Outline each blood parasite and name the species.
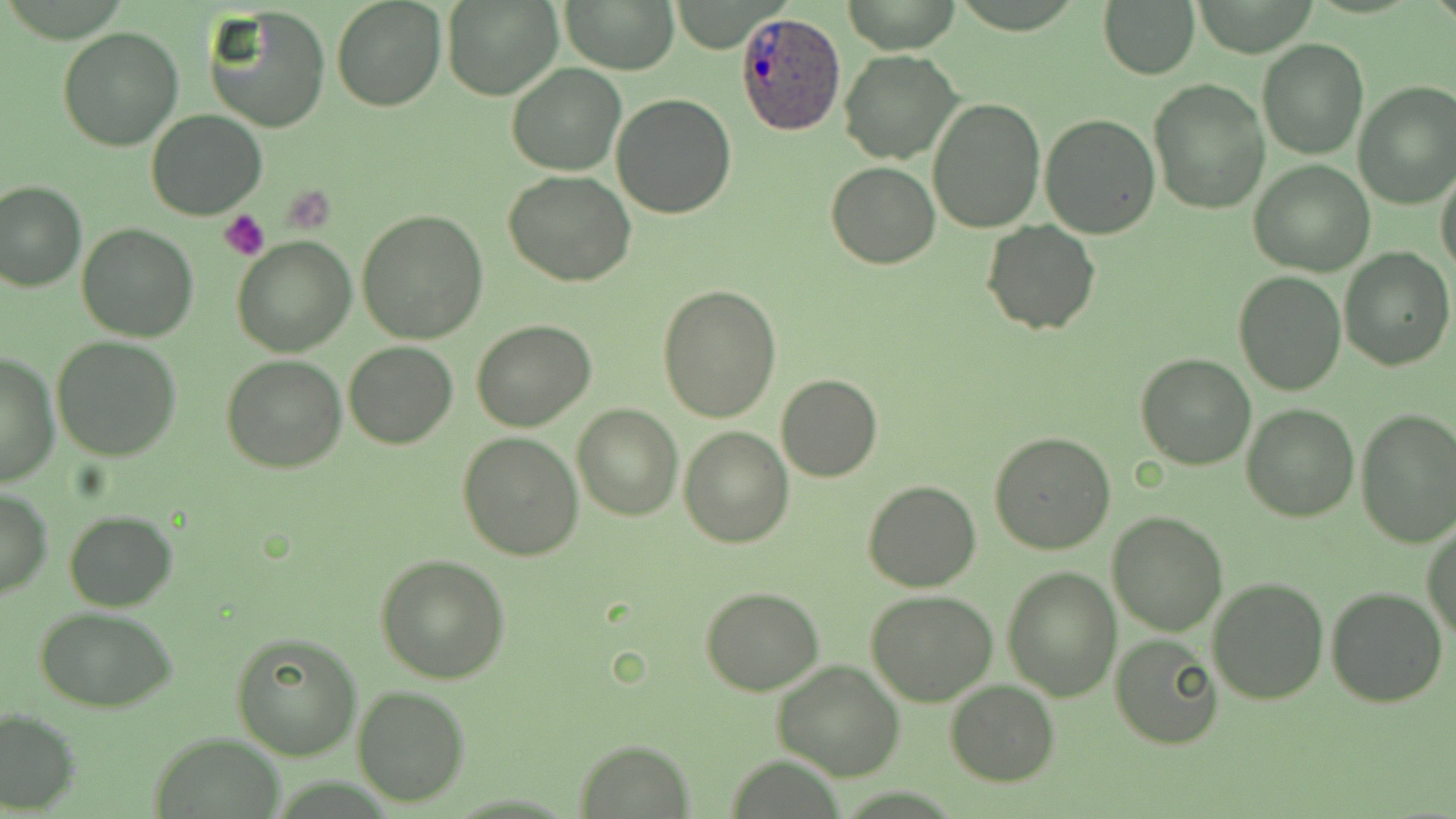

Approximate bounding boxes as (x1, y1, x2, y2) in pixels.
Plasmodium ovale-infected red blood cells: (738, 9, 845, 134).
No Plasmodium falciparum, Plasmodium malariae, Plasmodium vivax, Babesia divergens, or Trypanosoma brucei observed.

Summary:
  - Uninfected red blood cell locations: (561, 0, 678, 75), (1098, 0, 1201, 80), (332, 1, 445, 111), (442, 1, 561, 100), (837, 1, 962, 53), (204, 5, 331, 134), (58, 27, 183, 150), (1257, 38, 1369, 159), (838, 50, 962, 165), (506, 63, 626, 176), (1149, 78, 1269, 214), (1353, 82, 1456, 210), (611, 93, 736, 219), (929, 96, 1045, 231), (147, 110, 266, 220), (1040, 115, 1160, 239), (1249, 161, 1375, 276), (827, 163, 940, 268), (1435, 166, 1456, 280), (503, 171, 636, 289), (1, 180, 85, 292), (357, 208, 489, 343), (983, 220, 1099, 335), (77, 224, 199, 342), (232, 236, 356, 357), (1339, 247, 1454, 370), (1233, 272, 1345, 396), (659, 282, 782, 423), (471, 320, 596, 433), (53, 336, 182, 460), (344, 341, 457, 449), (1, 351, 58, 487), (1135, 354, 1257, 472), (222, 356, 348, 474), (775, 373, 882, 481), (1242, 402, 1359, 521), (573, 403, 682, 520), (1355, 408, 1456, 548), (678, 427, 793, 549), (458, 432, 584, 560), (987, 432, 1115, 555), (863, 479, 981, 592), (0, 487, 52, 598), (64, 510, 178, 611), (1106, 511, 1229, 635), (1423, 520, 1455, 642), (375, 554, 512, 684), (1002, 567, 1121, 702), (1208, 576, 1328, 703), (699, 587, 824, 696), (1326, 587, 1447, 708), (866, 590, 998, 706), (35, 607, 179, 712), (232, 632, 362, 761), (1111, 633, 1223, 749), (772, 660, 905, 781), (945, 679, 1061, 785), (353, 686, 470, 806), (1, 707, 79, 814), (150, 733, 285, 817), (575, 740, 692, 815)
  - Platelet locations: (284, 189, 334, 235), (219, 209, 270, 261)
  - Slide-level diagnosis: Plasmodium ovale
  - Field of view: single
  - Stain: May-Grünwald-Giemsa
  - Magnification: 1000x
  - Image size: 1456×819 pixels
  - Modality: optical microscopy
  - Preparation: thin blood smear